Outline each blood parasite and name the species.
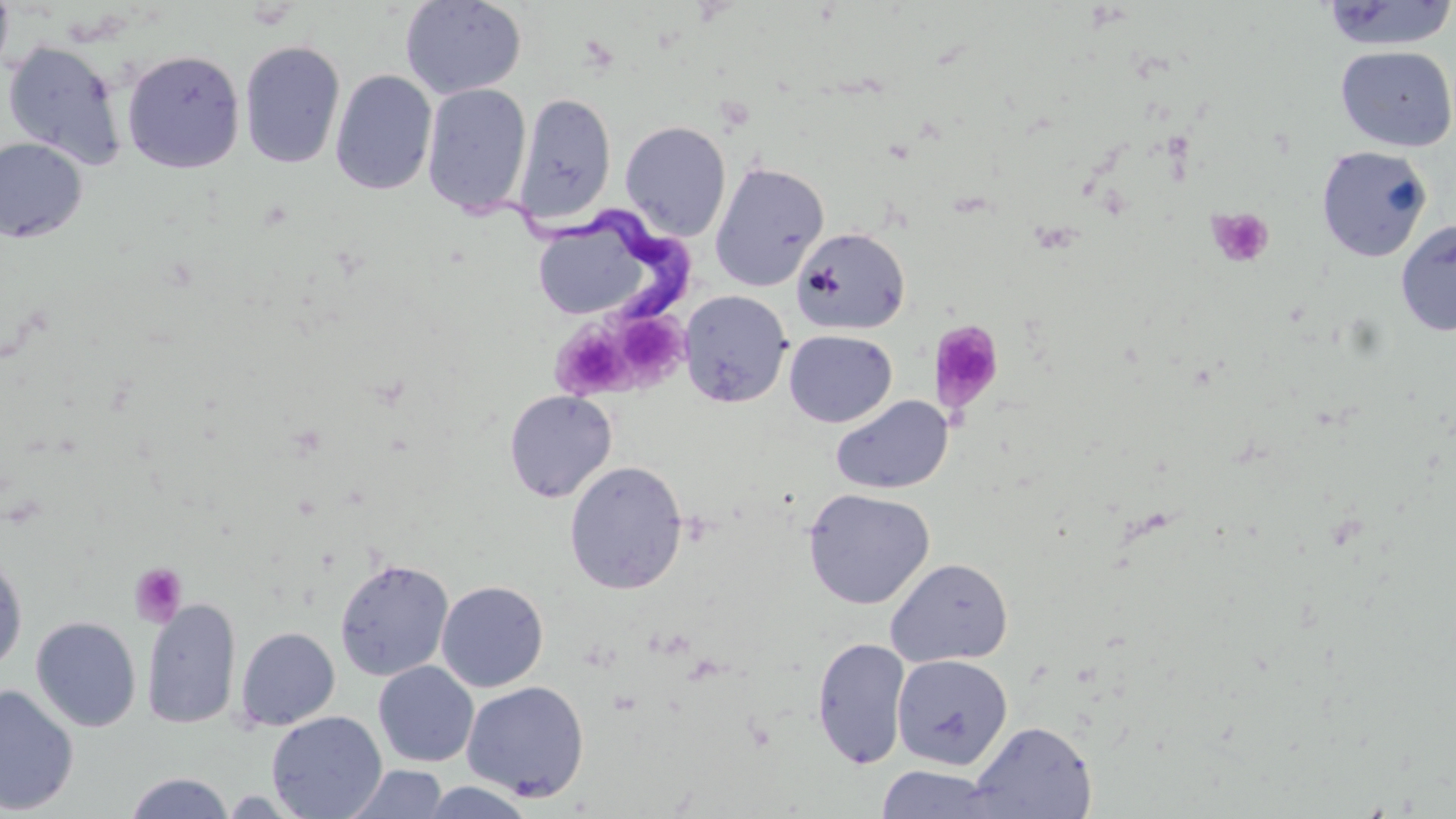
Approximate bounding boxes as named x1/y1/x2/y2 corners in pixels.
Trypanosoma brucei: (x1=476, y1=191, x2=690, y2=324).
No Plasmodium falciparum, Plasmodium ovale, Plasmodium malariae, Plasmodium vivax, or Babesia divergens observed.

Summary:
  - Uninfected red blood cell locations: (x1=0, y1=0, x2=14, y2=81), (x1=1318, y1=0, x2=1456, y2=53), (x1=399, y1=1, x2=527, y2=99), (x1=2, y1=40, x2=129, y2=171), (x1=239, y1=40, x2=346, y2=169), (x1=1334, y1=45, x2=1456, y2=152), (x1=121, y1=49, x2=246, y2=174), (x1=330, y1=69, x2=438, y2=196), (x1=422, y1=83, x2=532, y2=215), (x1=514, y1=93, x2=616, y2=224), (x1=512, y1=106, x2=732, y2=231), (x1=620, y1=120, x2=731, y2=241), (x1=0, y1=137, x2=88, y2=243), (x1=1316, y1=146, x2=1433, y2=262), (x1=710, y1=161, x2=830, y2=292), (x1=527, y1=213, x2=650, y2=323), (x1=1395, y1=218, x2=1456, y2=337), (x1=792, y1=227, x2=910, y2=335), (x1=679, y1=290, x2=792, y2=408), (x1=783, y1=329, x2=897, y2=428), (x1=504, y1=389, x2=618, y2=503), (x1=830, y1=394, x2=954, y2=495), (x1=564, y1=460, x2=688, y2=595), (x1=802, y1=488, x2=935, y2=609), (x1=0, y1=548, x2=28, y2=674), (x1=886, y1=557, x2=1014, y2=668), (x1=334, y1=558, x2=454, y2=681), (x1=436, y1=580, x2=549, y2=692), (x1=142, y1=597, x2=242, y2=730), (x1=30, y1=616, x2=142, y2=732), (x1=235, y1=627, x2=340, y2=730), (x1=812, y1=637, x2=911, y2=769), (x1=891, y1=654, x2=1013, y2=770), (x1=373, y1=661, x2=479, y2=767), (x1=461, y1=680, x2=590, y2=802), (x1=0, y1=683, x2=80, y2=815), (x1=267, y1=711, x2=387, y2=819), (x1=968, y1=720, x2=1098, y2=819), (x1=343, y1=764, x2=449, y2=818), (x1=874, y1=764, x2=1003, y2=819), (x1=123, y1=772, x2=236, y2=818), (x1=419, y1=781, x2=536, y2=818)
  - Platelet locations: (x1=1206, y1=207, x2=1275, y2=269), (x1=551, y1=312, x2=678, y2=401), (x1=929, y1=320, x2=1005, y2=415), (x1=129, y1=562, x2=188, y2=627)
  - Slide-level diagnosis: Trypanosoma brucei
  - Magnification: 1000x
  - Stain: May-Grünwald-Giemsa
  - Image size: 1456×819 pixels
  - Preparation: thin blood film
  - Modality: optical microscopy
  - Field of view: one of a larger specimen